Report the malaria status of this cell.
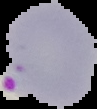
Parasitized.

Summary:
  - Preparation: thin blood film
  - Image size: 97×109 pixels
  - Image type: segmented cell region on a black background